Assess the morphology of the red blood cells.
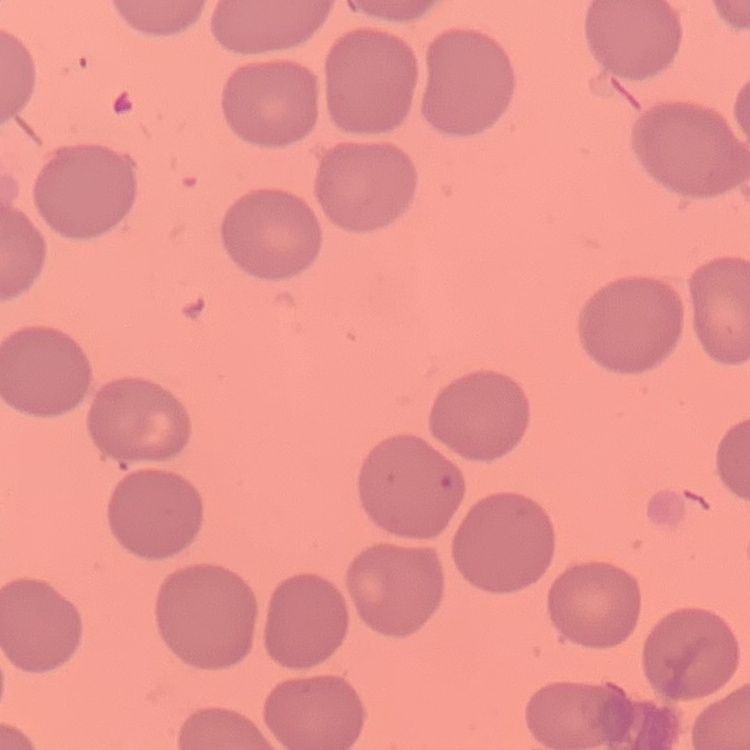

No rouleaux formation.

One tile cut from a larger photomicrograph. Field's or Giemsa stain. Thin peripheral smear.